Describe the morphology of the red blood cells.
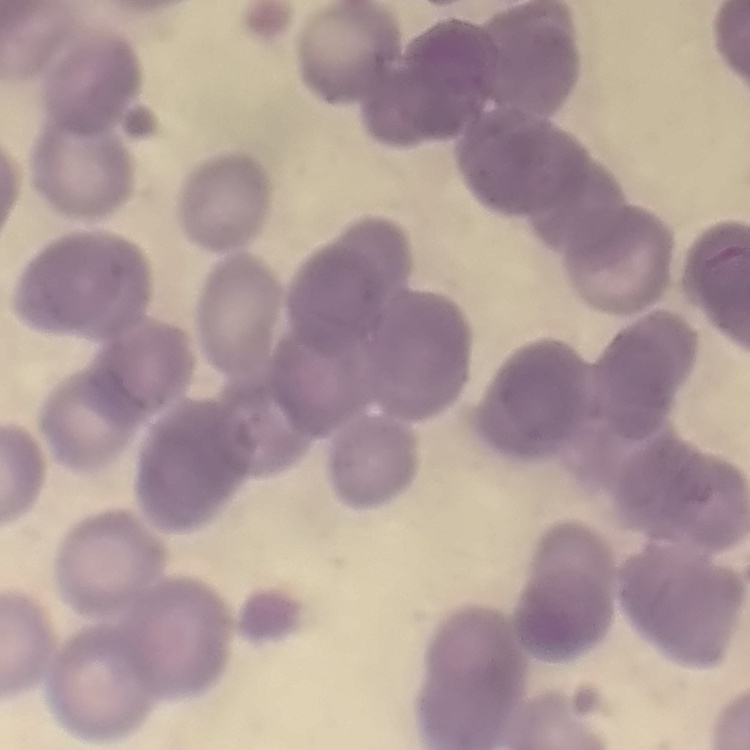

Rouleaux formation.

Field's or Giemsa stain. Thin peripheral smear. Square crop of a larger photomicrograph.